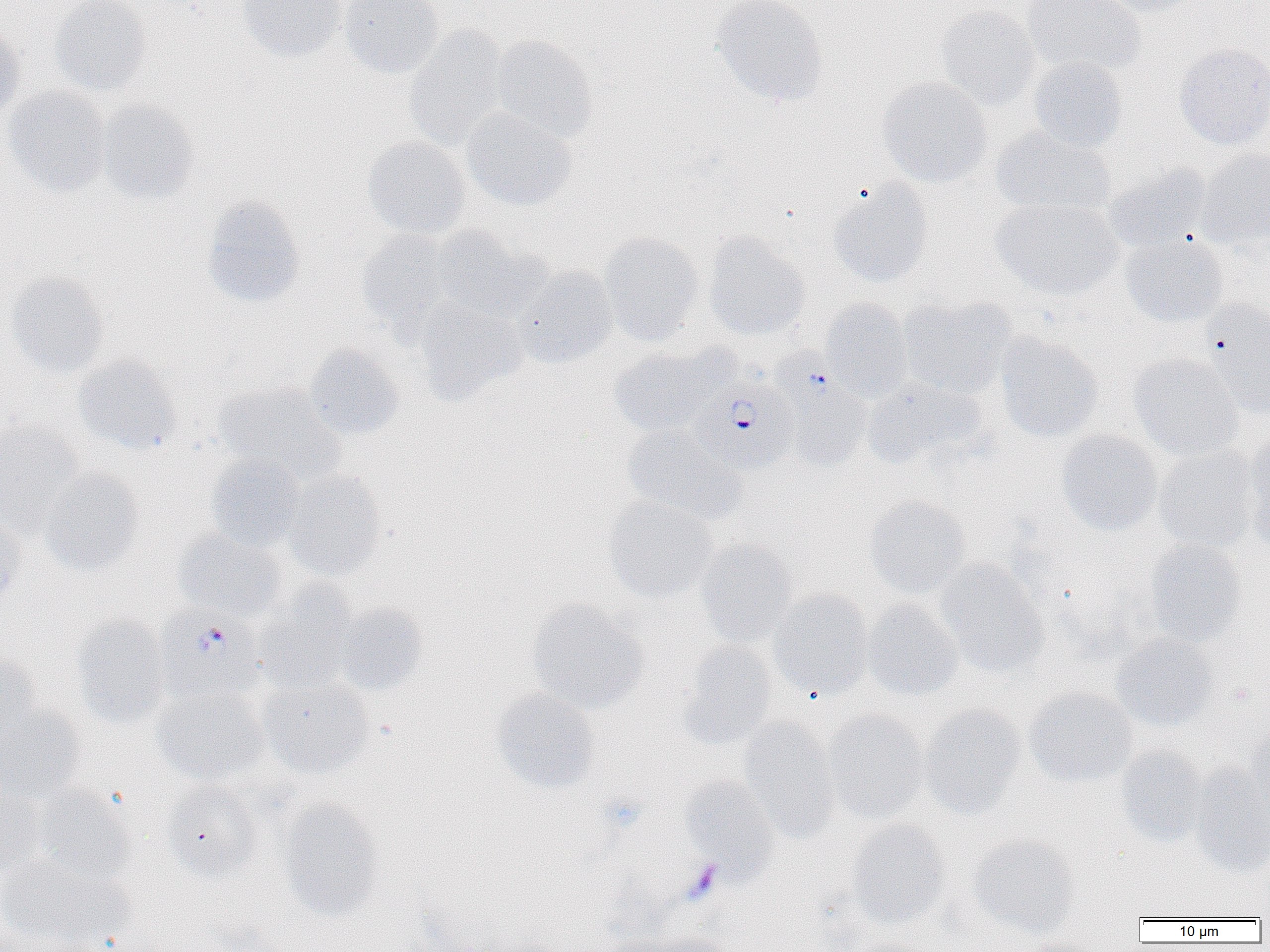

Summary:
  - Coordinate format: approximate bounding boxes as (x1,y1)-(x2,y2) corner pairs in pixels
  - Uninfected red blood cell locations: (50,0)-(152,96), (237,0)-(345,62), (340,0)-(444,79), (711,0)-(829,108), (1022,0)-(1145,77), (1104,0)-(1202,17), (935,5)-(1041,110), (403,25)-(510,149), (0,26)-(25,121), (491,34)-(598,142), (1174,43)-(1270,150), (1028,56)-(1127,153), (876,76)-(994,186), (4,86)-(111,196), (96,100)-(199,204), (460,107)-(577,212), (990,125)-(1116,219), (361,126)-(574,224), (362,136)-(471,239), (1197,147)-(1270,247), (1103,164)-(1210,252), (827,178)-(933,288), (201,195)-(305,308), (992,197)-(1123,300), (430,224)-(542,321), (356,229)-(459,332), (599,232)-(705,346), (1121,232)-(1228,327), (704,234)-(809,340), (513,267)-(617,368), (5,271)-(109,379), (898,296)-(1016,397), (820,298)-(912,400), (415,299)-(525,404), (1202,301)-(1270,421), (996,332)-(1104,442), (304,343)-(404,440), (608,343)-(730,436), (73,354)-(182,456), (1128,354)-(1244,460), (863,377)-(985,470), (213,382)-(344,484), (790,388)-(872,471), (0,420)-(85,536), (621,424)-(745,525), (1056,429)-(1162,536), (1241,436)-(1270,550), (1153,445)-(1259,552), (207,454)-(306,551), (39,468)-(145,576), (285,471)-(387,581), (863,495)-(971,599), (603,496)-(719,603), (0,511)-(25,608), (173,529)-(287,622), (695,539)-(797,648), (1142,539)-(1246,646), (935,559)-(1049,678), (253,583)-(358,693), (769,589)-(874,700), (527,599)-(648,714), (862,599)-(963,700), (334,603)-(428,696), (71,612)-(171,726), (1111,633)-(1219,732), (675,641)-(777,749), (0,655)-(42,747), (258,675)-(374,777), (153,687)-(270,785), (490,688)-(601,794), (1024,688)-(1137,787), (920,704)-(1027,819), (0,709)-(85,803), (823,709)-(930,823), (738,717)-(840,842), (1246,725)-(1269,818), (1115,745)-(1209,847), (1190,766)-(1270,876), (680,774)-(780,877), (162,781)-(264,882), (34,785)-(137,883), (0,787)-(45,878), (276,799)-(385,921), (846,820)-(951,930), (967,834)-(1081,936), (0,855)-(130,950), (0,922)-(44,952), (643,933)-(733,952), (597,936)-(684,952)
  - Plasmodium falciparum-infected red blood cell locations: (764,347)-(870,467), (693,372)-(799,473), (154,608)-(268,703)
  - Platelet locations: (682,860)-(723,904)
  - Slide-level diagnosis: Plasmodium falciparum
  - Magnification: 1000x
  - Image size: 1270×952 pixels
  - Preparation: thin blood film
  - Modality: light microscopy
  - Field of view: single